Comment on the morphology of the erythrocytes.
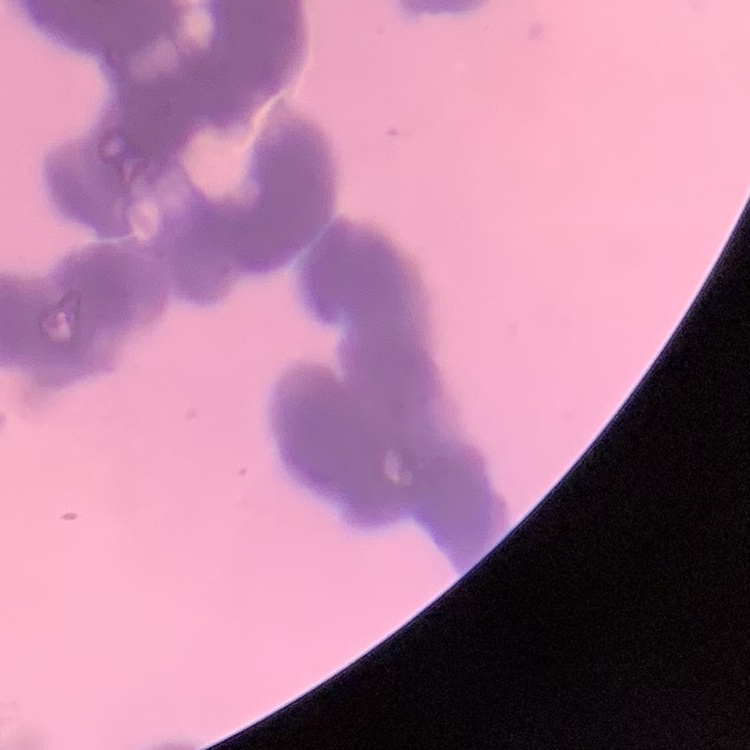
Rouleaux formation.

image type = square crop of a larger photomicrograph
stain = Field's or Giemsa
preparation = thin blood film